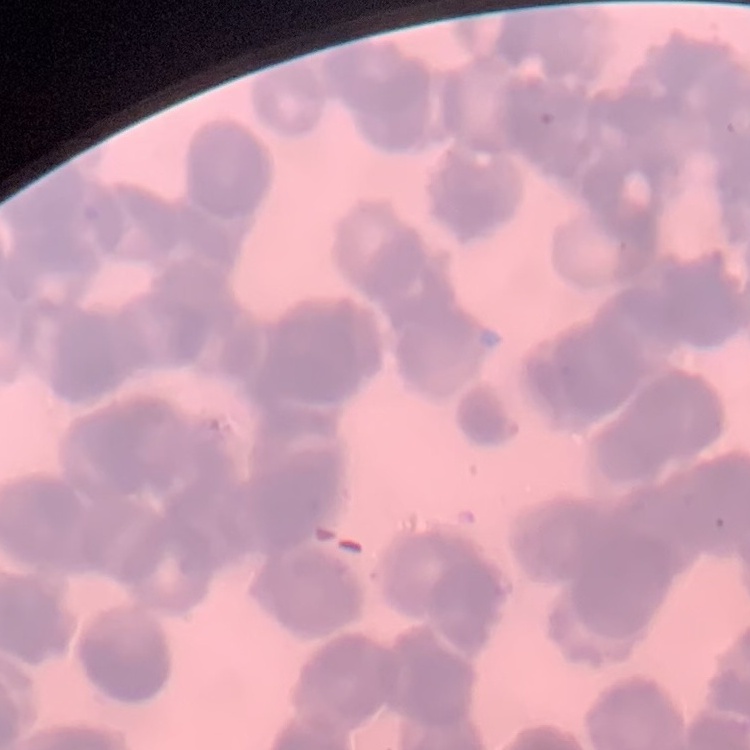
The red blood cells exhibit rouleaux formation. One tile cut from a larger photomicrograph. Thin peripheral smear. Stained with either Field's or Giemsa.